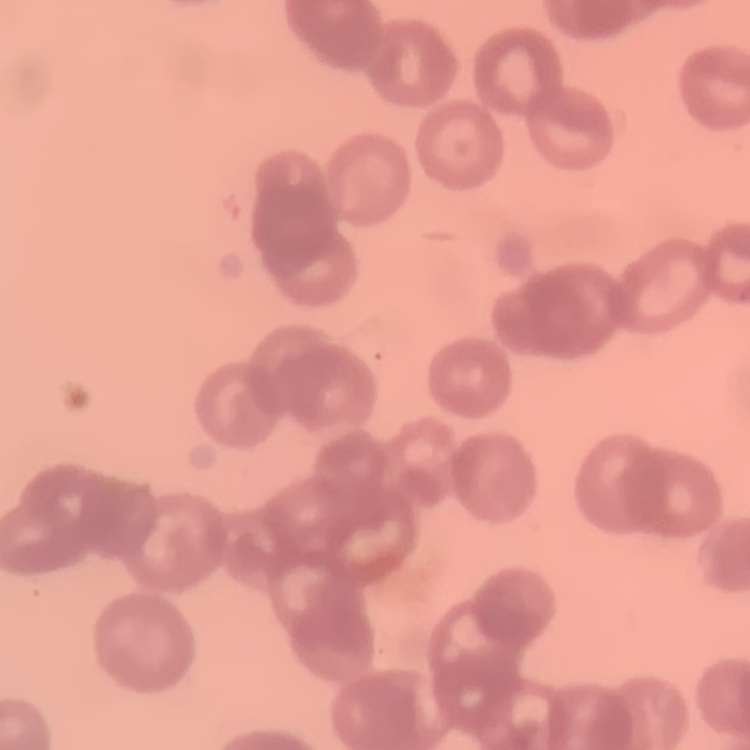

red blood cell morphology = rouleaux formation
preparation = thin blood film
image type = square crop of a larger photomicrograph
stain = Field's or Giemsa